Identify the cell.
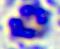
This is a leukocyte.

modality = photomicrograph
magnification = 400x